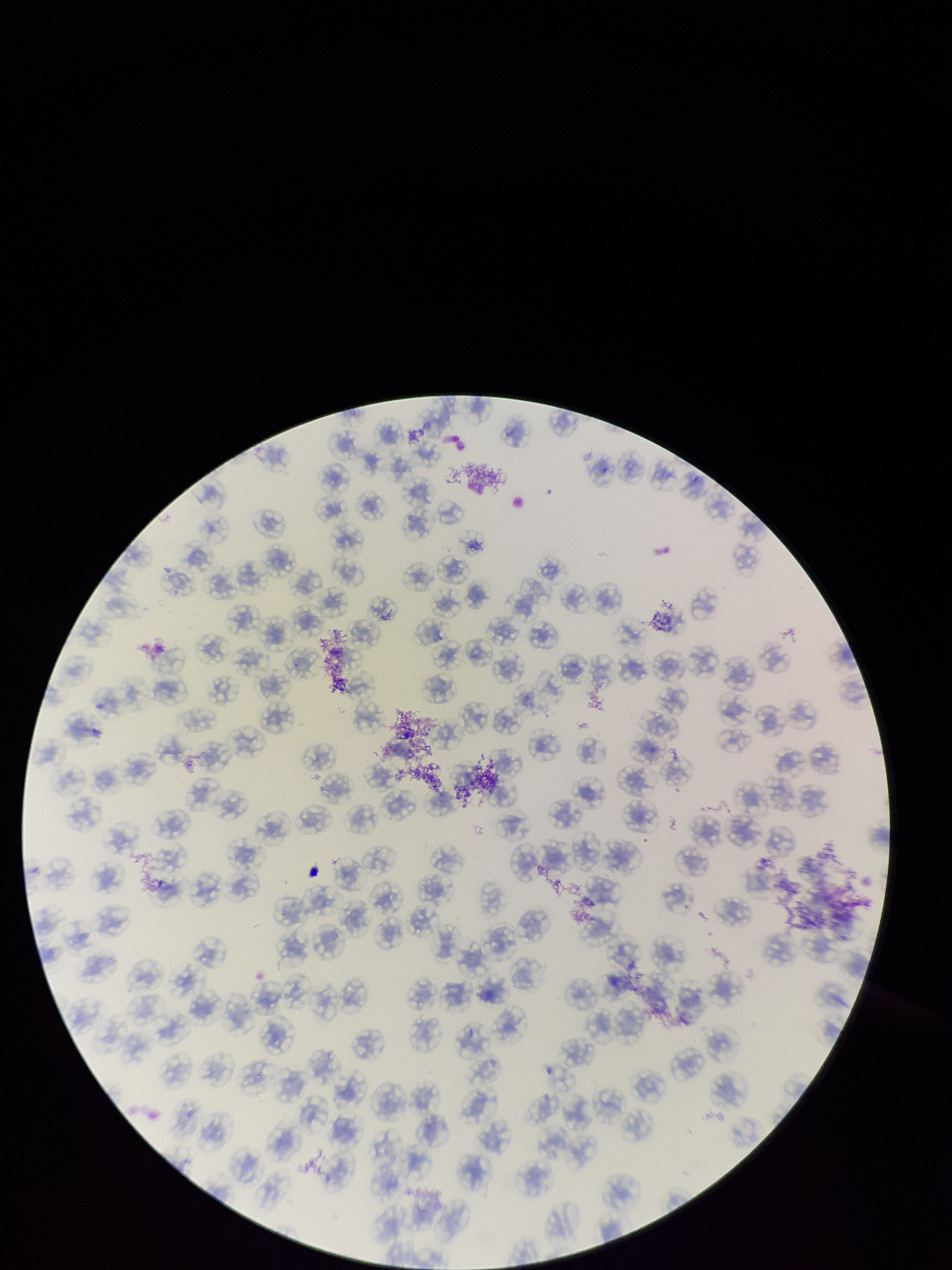
red blood cell count = 108
preparation = thin
field of view = one from this slide
image size = 952×1270 pixels
stain = Giemsa
patient malaria status = negative
parasitized red blood cell count = 0
parasitized red blood cells = none identified
capture = smartphone photograph through the microscope eyepiece